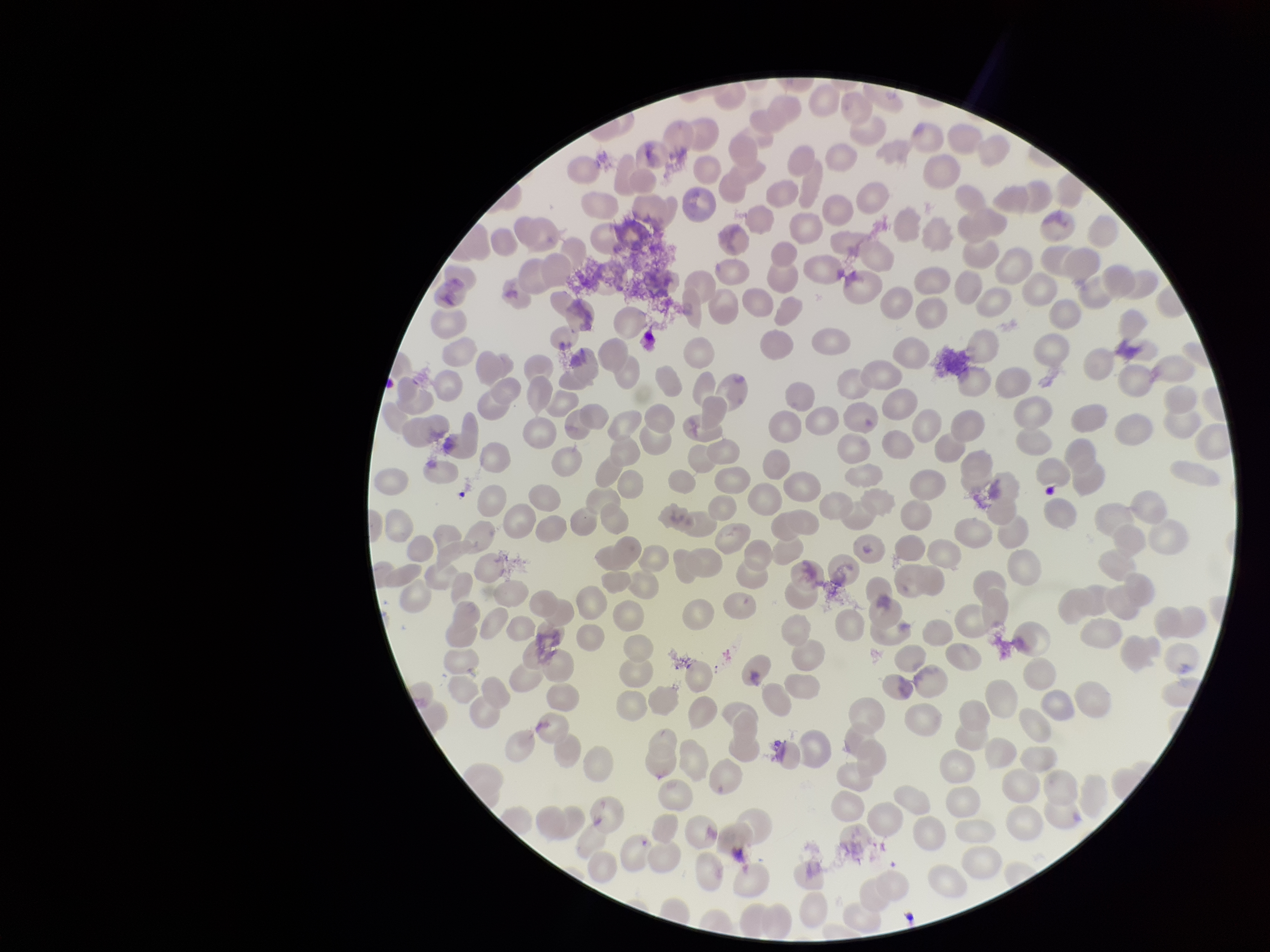

image size = 1270×952 pixels
stain = Giemsa
parasitized red blood cell count = 0
parasitized red blood cells = none seen
field of view = single
patient malaria status = infected
preparation = thin
red blood cell count = 245
species reported for this patient = Plasmodium falciparum
capture = smartphone photograph through the microscope eyepiece